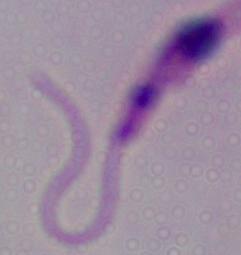

Summary:
  - Magnification: 1000x
  - Identification: Leishmania
  - Modality: photomicrograph